Locate every malaria parasite and every leukocyte.
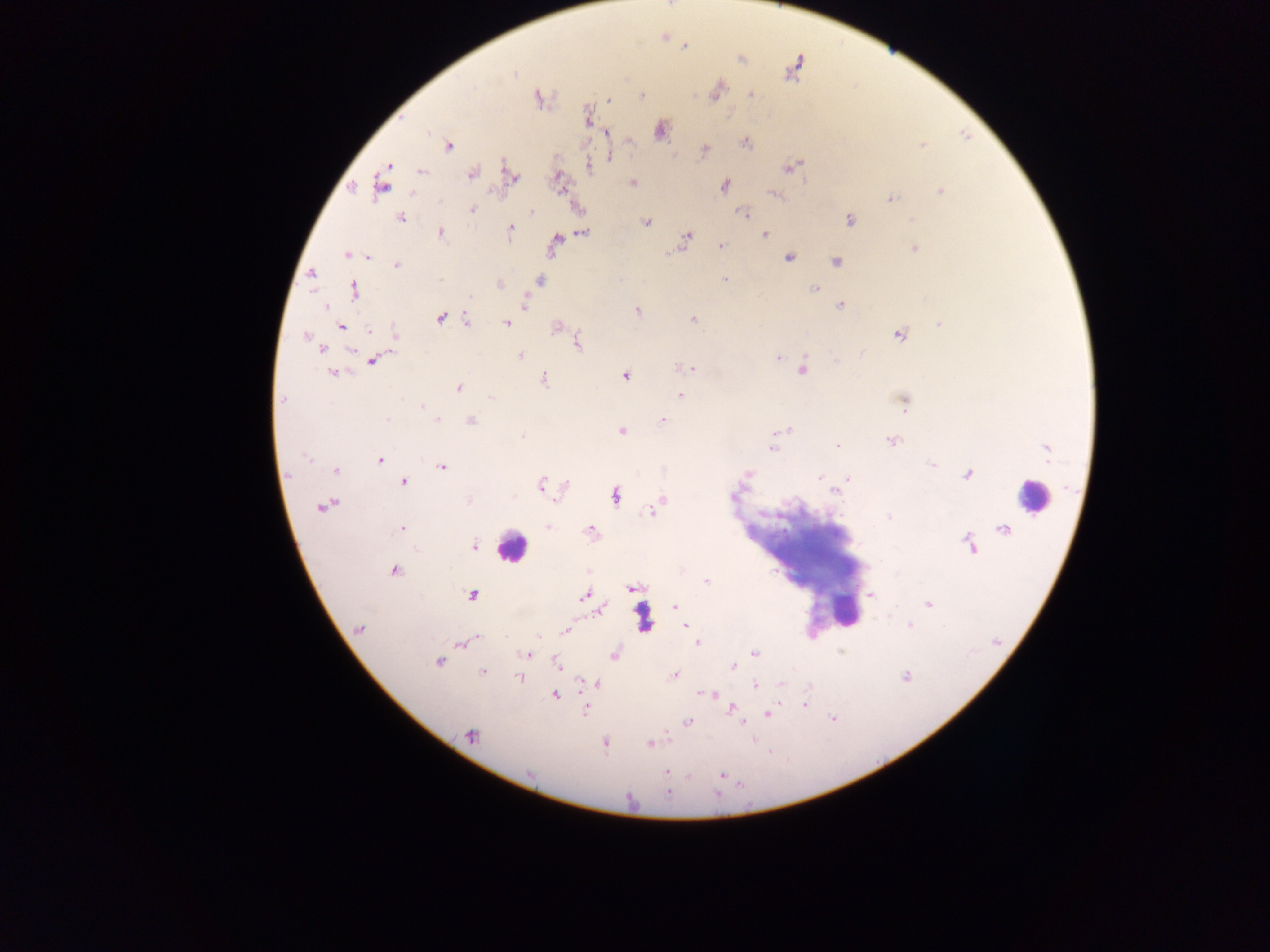

Approximate centers as [x, y] in pixels.
Malaria parasites: [684, 46], [742, 59], [792, 71], [514, 74], [717, 92], [751, 95], [642, 96], [538, 98], [608, 100], [588, 118], [661, 131], [607, 134], [745, 143], [923, 145], [449, 146], [704, 150], [610, 157], [793, 166], [588, 167], [422, 172], [471, 174], [512, 177], [381, 182], [632, 183], [724, 186], [940, 191], [773, 194], [890, 199], [473, 209], [531, 212], [743, 214], [400, 218], [850, 220], [647, 222], [510, 230], [584, 232], [441, 233], [765, 235], [687, 236], [555, 244], [721, 246], [915, 249], [669, 253], [347, 254], [369, 257], [789, 258], [837, 261], [396, 265], [311, 274], [440, 279], [724, 279], [539, 280], [500, 284], [814, 288], [354, 291], [470, 297], [524, 304], [840, 304], [325, 307], [637, 311], [441, 319], [692, 319], [466, 320], [506, 323], [939, 324], [557, 325], [340, 327], [370, 330], [396, 332], [899, 335], [306, 336], [577, 344], [322, 350], [520, 356], [778, 358], [373, 360], [690, 368], [802, 370], [333, 373], [625, 375], [544, 379], [459, 389], [680, 395], [491, 397], [282, 399], [905, 403], [422, 406], [387, 419], [437, 420], [663, 420], [471, 421], [787, 429], [622, 431], [522, 436], [892, 442], [837, 445], [773, 447], [1048, 451], [305, 458], [379, 460], [932, 465], [442, 467], [335, 470], [747, 473], [967, 474], [820, 477], [849, 479], [403, 482], [541, 484], [837, 491], [734, 495], [616, 496], [662, 499], [557, 500], [469, 501], [659, 505], [323, 507], [651, 512], [889, 517], [548, 527], [401, 529], [590, 531], [969, 545], [475, 546], [395, 571], [706, 581], [632, 588], [471, 595], [585, 595], [871, 595], [928, 604], [675, 607], [601, 610], [909, 625], [685, 626], [360, 628], [566, 631], [538, 637], [476, 638], [470, 640], [462, 643], [697, 643], [754, 653], [527, 655], [614, 656], [438, 662], [556, 665], [734, 667], [482, 671], [674, 675], [906, 676], [519, 677], [598, 683], [782, 684], [756, 685], [706, 694], [555, 695], [804, 705], [731, 709], [586, 710], [768, 714], [688, 721], [471, 736], [605, 744], [649, 744], [666, 772], [722, 775], [669, 793].
Leukocytes: [1032, 497], [511, 546], [844, 608], [641, 614].

Thick blood smear. Mobile-phone photograph taken through the microscope. Single field of view. Collected in Ghana. Image is 1270×952 pixels.